Report the malaria status of this cell.
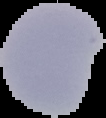
Uninfected.

Image is 106×118 pixels. From a thin blood smear. Segmented cell region on a black background.